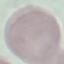
Malaria status: uninfected. Giemsa stain. Thin blood smear. Automatically extracted cell patch, resized to 64 × 64 pixels. Photographed with a smartphone camera at the microscope eyepiece.